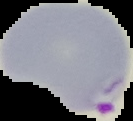
{
  "malaria_status": "parasitized",
  "image_size": "133×121 pixels",
  "preparation": "thin blood film",
  "image_type": "segmented cell region with the area outside set to black"
}